Identify the blood parasite species.
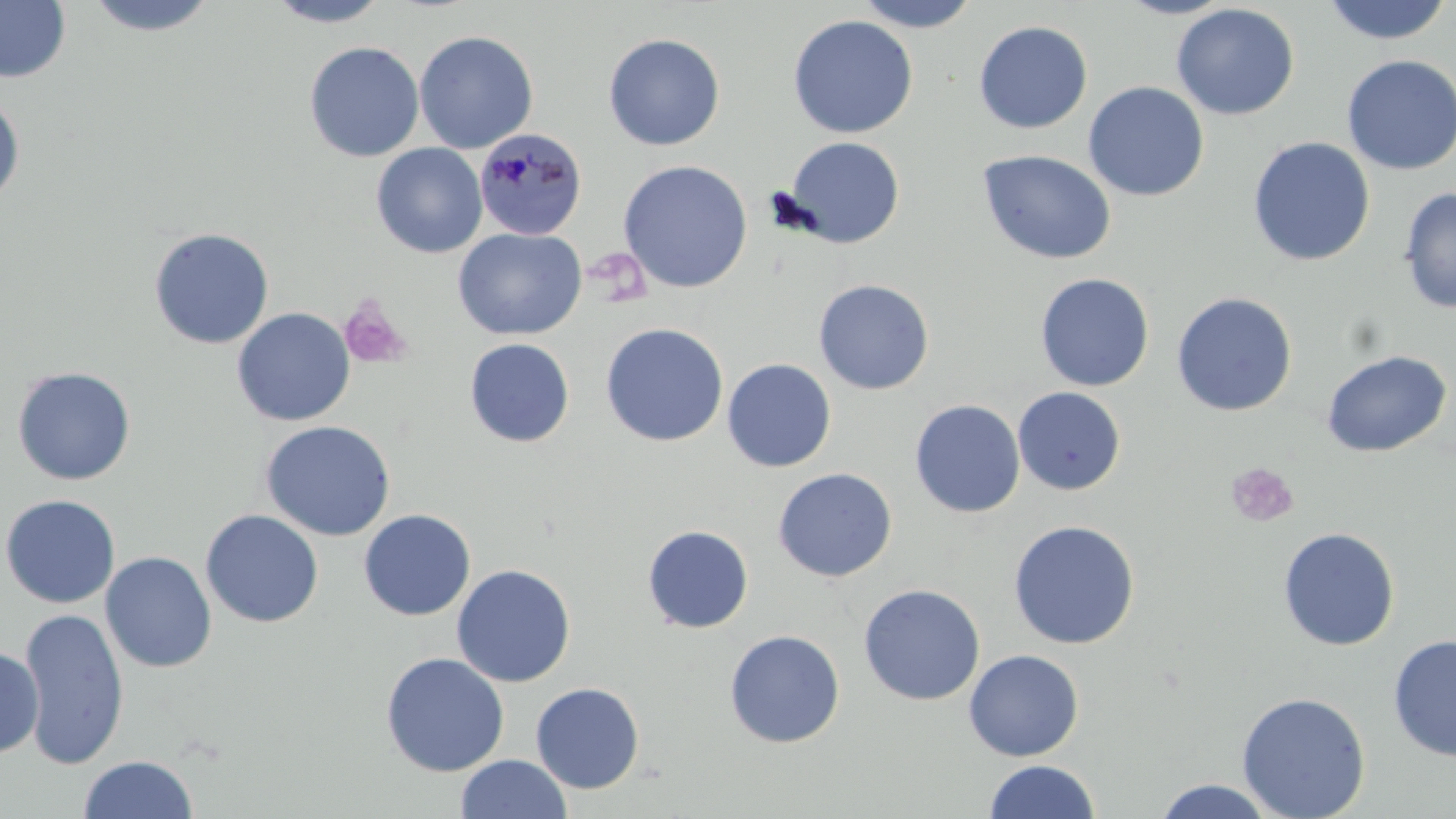
Plasmodium malariae.

Summary:
  - Coordinate format: approximate bounding boxes as named x1/y1/x2/y2 corners in pixels
  - Platelet locations: (x1=338, y1=293, x2=412, y2=371), (x1=1225, y1=462, x2=1299, y2=527)
  - Plasmodium malariae-infected red blood cell locations: (x1=475, y1=132, x2=588, y2=244)
  - Uninfected red blood cell locations: (x1=0, y1=0, x2=71, y2=84), (x1=80, y1=0, x2=221, y2=38), (x1=265, y1=0, x2=391, y2=27), (x1=851, y1=0, x2=981, y2=33), (x1=1114, y1=0, x2=1238, y2=19), (x1=1320, y1=0, x2=1454, y2=45), (x1=1171, y1=3, x2=1300, y2=120), (x1=787, y1=15, x2=919, y2=139), (x1=973, y1=20, x2=1093, y2=134), (x1=414, y1=30, x2=538, y2=154), (x1=603, y1=33, x2=726, y2=151), (x1=304, y1=41, x2=424, y2=162), (x1=1341, y1=53, x2=1456, y2=176), (x1=1083, y1=81, x2=1209, y2=201), (x1=0, y1=93, x2=26, y2=208), (x1=782, y1=136, x2=905, y2=249), (x1=1247, y1=136, x2=1375, y2=267), (x1=371, y1=143, x2=488, y2=258), (x1=977, y1=149, x2=1117, y2=265), (x1=618, y1=160, x2=753, y2=293), (x1=1398, y1=186, x2=1456, y2=314), (x1=148, y1=227, x2=275, y2=350), (x1=453, y1=227, x2=587, y2=340), (x1=1035, y1=272, x2=1155, y2=392), (x1=814, y1=280, x2=934, y2=395), (x1=1171, y1=292, x2=1297, y2=417), (x1=231, y1=307, x2=356, y2=427), (x1=600, y1=322, x2=728, y2=447), (x1=464, y1=338, x2=575, y2=448), (x1=1321, y1=349, x2=1453, y2=458), (x1=721, y1=358, x2=837, y2=472), (x1=12, y1=366, x2=136, y2=486), (x1=1012, y1=387, x2=1127, y2=495), (x1=909, y1=399, x2=1026, y2=518), (x1=259, y1=420, x2=396, y2=541), (x1=773, y1=468, x2=897, y2=582), (x1=0, y1=494, x2=121, y2=609), (x1=200, y1=509, x2=324, y2=628), (x1=358, y1=509, x2=476, y2=621), (x1=1007, y1=519, x2=1140, y2=649), (x1=642, y1=525, x2=754, y2=634), (x1=1278, y1=527, x2=1400, y2=651), (x1=100, y1=551, x2=217, y2=673), (x1=451, y1=564, x2=575, y2=687), (x1=859, y1=584, x2=985, y2=706), (x1=19, y1=606, x2=129, y2=770), (x1=724, y1=629, x2=846, y2=748), (x1=1387, y1=634, x2=1456, y2=762), (x1=0, y1=646, x2=44, y2=759), (x1=963, y1=649, x2=1084, y2=761), (x1=380, y1=652, x2=509, y2=777), (x1=530, y1=681, x2=645, y2=794), (x1=1236, y1=691, x2=1371, y2=819), (x1=78, y1=754, x2=198, y2=818), (x1=455, y1=754, x2=572, y2=818), (x1=983, y1=759, x2=1101, y2=818), (x1=1151, y1=779, x2=1281, y2=818)
  - Image size: 1456×819 pixels
  - Magnification: 1000x
  - Stain: May-Grünwald-Giemsa
  - Field of view: single
  - Modality: optical microscopy
  - Preparation: thin blood smear